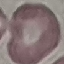
malaria_status: uninfected
capture: smartphone camera at the microscope eyepiece
image_type: automatically extracted cell patch, resized to 64 × 64 pixels
preparation: thin smear
stain: Giemsa